State which parasite is depicted.
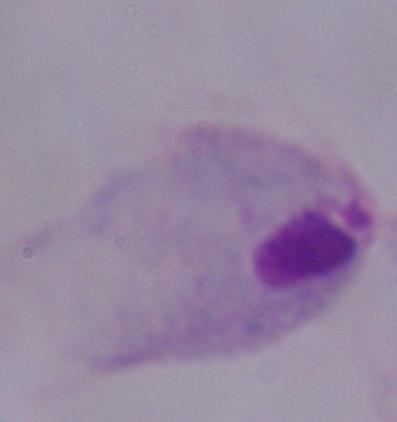

This is a trichomonad.

modality: micrograph
magnification: 1000x